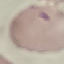

Summary:
  - Malaria status: parasitized
  - Stain: Giemsa
  - Image type: automatically extracted cell patch, resized to 64 × 64 pixels
  - Capture: smartphone camera at the microscope eyepiece
  - Preparation: thin blood smear